Classify this cell by malaria status.
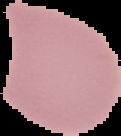
It is uninfected.

preparation: thin blood film
image_type: segmented cell region on a black background
image_size: 121×136 pixels